State which parasite is depicted.
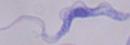

This is a trypanosome.

magnification: 1000x
modality: micrograph